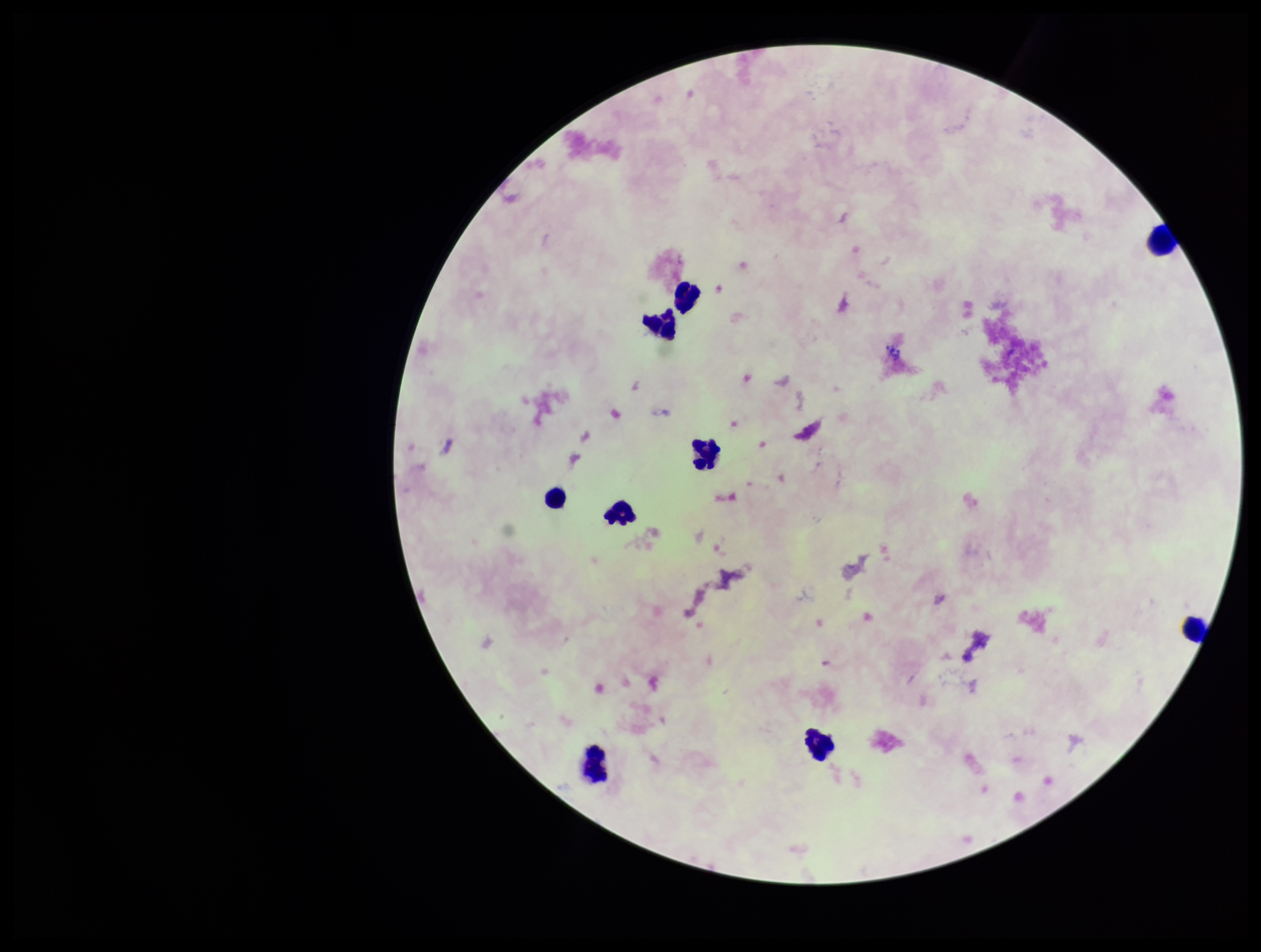

Summary:
  - Image size: 1261×952 pixels
  - Parasite count: 0
  - Leukocyte count: 9
  - Stain: Giemsa
  - Plasmodium parasites: none identified
  - Patient malaria status: negative
  - Capture: smartphone photograph through the microscope eyepiece
  - Preparation: thick blood smear
  - Field of view: one from this slide